Assess this cell for malaria.
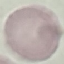
Uninfected.

stain = Giemsa
image type = automatically extracted cell patch, resized to 64 × 64 pixels
capture = smartphone camera at the microscope eyepiece
preparation = thin blood smear